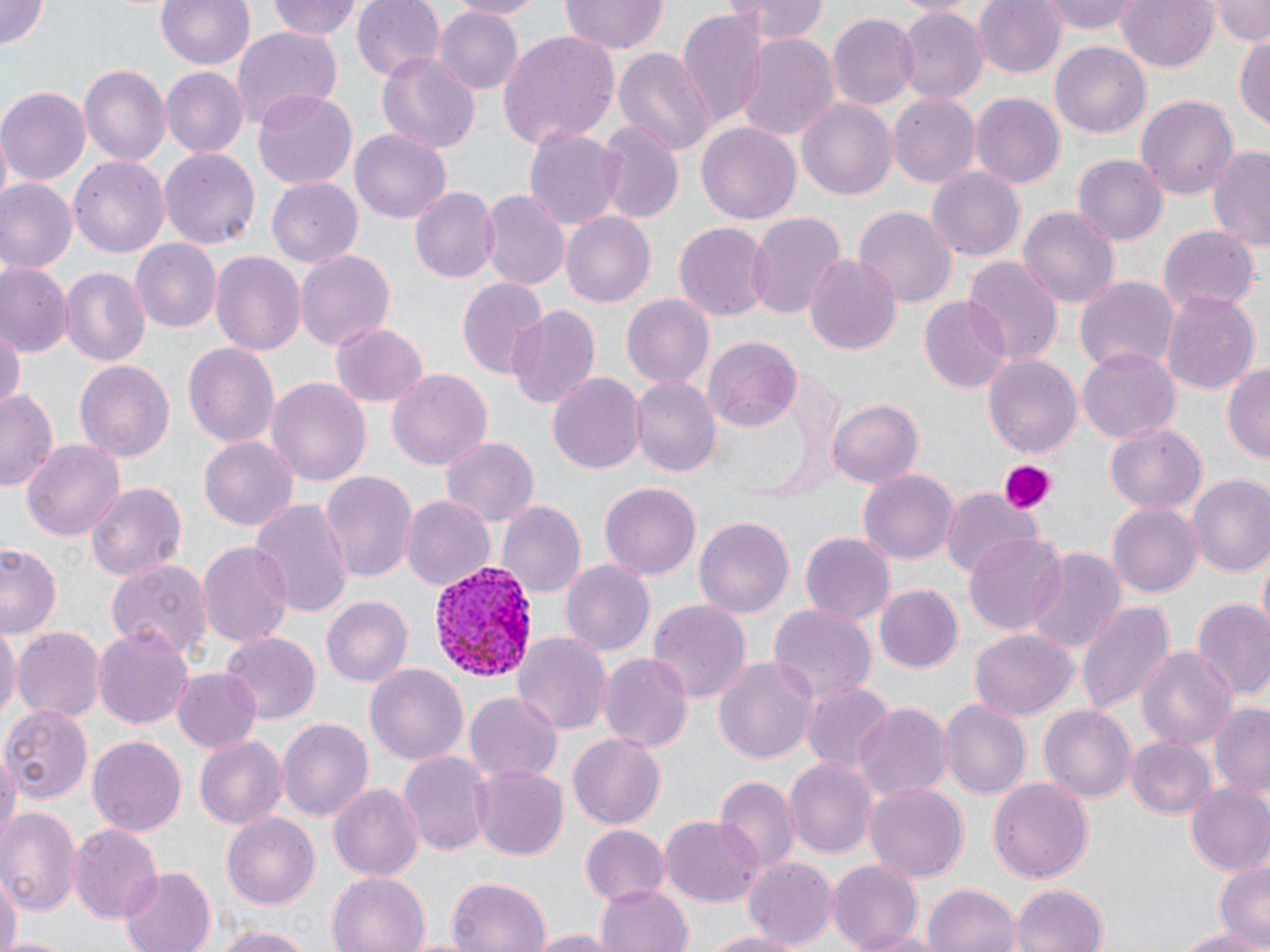
slide-level diagnosis = Plasmodium vivax
uninfected red blood cell locations = approximate bounding boxes as (x1, y1, x2, y2) in pixels: (0, 0, 53, 50), (154, 0, 257, 70), (266, 0, 361, 40), (352, 0, 446, 81), (450, 0, 544, 19), (562, 0, 666, 55), (738, 0, 827, 45), (975, 0, 1067, 79), (1039, 0, 1144, 35), (1116, 0, 1218, 73), (1213, 0, 1270, 44), (675, 5, 768, 125), (896, 5, 988, 104), (436, 7, 523, 94), (827, 13, 918, 112), (231, 25, 343, 128), (1235, 30, 1270, 130), (497, 31, 621, 145), (734, 33, 839, 144), (1051, 41, 1149, 139), (612, 47, 716, 155), (376, 54, 479, 154), (79, 63, 170, 165), (160, 68, 247, 156), (0, 85, 90, 185), (251, 90, 358, 191), (972, 92, 1064, 187), (1136, 94, 1238, 202), (888, 95, 979, 188), (797, 97, 896, 202), (596, 120, 685, 225), (697, 122, 801, 225), (524, 124, 624, 230), (350, 129, 453, 225), (1207, 146, 1270, 252), (160, 147, 259, 250), (70, 154, 168, 254), (1074, 155, 1167, 246), (926, 166, 1025, 262), (266, 177, 363, 270), (1, 180, 76, 273), (410, 187, 499, 283), (481, 189, 569, 289), (854, 206, 957, 308), (1019, 206, 1119, 309), (562, 212, 656, 308), (744, 212, 847, 322), (674, 222, 769, 321), (1157, 224, 1259, 317), (132, 240, 222, 332), (209, 250, 307, 355), (294, 251, 394, 349), (804, 253, 902, 354), (960, 256, 1063, 368), (2, 265, 69, 357), (59, 266, 150, 368), (456, 276, 549, 382), (1075, 276, 1178, 374), (1162, 291, 1259, 395), (623, 295, 713, 389), (920, 296, 1012, 393), (507, 305, 600, 411), (0, 319, 23, 417), (329, 321, 429, 406), (704, 335, 801, 431), (182, 340, 281, 452), (1077, 346, 1181, 443), (982, 351, 1084, 460), (73, 357, 175, 461), (1223, 360, 1270, 463), (387, 369, 492, 474), (548, 371, 645, 478), (630, 375, 719, 477), (266, 377, 372, 488), (0, 389, 59, 493), (829, 398, 923, 487), (1105, 422, 1207, 515), (440, 436, 540, 529), (200, 437, 296, 532), (22, 439, 124, 543), (859, 469, 957, 563), (321, 470, 417, 582), (1187, 475, 1270, 578), (85, 479, 187, 583), (600, 482, 701, 580), (942, 487, 1042, 582), (403, 496, 494, 594), (250, 499, 352, 618), (499, 502, 586, 601), (1107, 502, 1201, 599), (694, 515, 793, 617), (801, 533, 895, 623), (962, 534, 1068, 636), (197, 540, 294, 650), (0, 544, 63, 639), (1020, 546, 1128, 658), (1256, 555, 1269, 628), (105, 556, 213, 660), (561, 558, 655, 655), (873, 585, 961, 673), (322, 596, 412, 688), (1075, 598, 1173, 717), (646, 599, 752, 704), (1193, 600, 1270, 700), (766, 606, 876, 706), (0, 624, 19, 724), (93, 624, 195, 730), (12, 627, 104, 724), (514, 631, 612, 735), (970, 631, 1077, 722), (221, 633, 320, 722), (1138, 645, 1236, 750), (598, 649, 692, 751), (713, 653, 819, 768), (364, 663, 468, 766), (170, 668, 262, 755), (803, 682, 894, 773), (466, 693, 563, 785), (941, 699, 1029, 798), (853, 701, 953, 802), (1039, 703, 1135, 803), (1207, 703, 1270, 801), (1, 704, 92, 803), (278, 716, 374, 825), (568, 733, 666, 829), (194, 734, 288, 829), (88, 736, 185, 838), (1125, 737, 1216, 819), (1, 744, 17, 852), (399, 750, 491, 857), (784, 757, 879, 860), (471, 763, 567, 858), (711, 773, 799, 874), (990, 777, 1093, 882), (329, 782, 425, 882), (864, 783, 969, 882), (1185, 783, 1270, 877), (0, 807, 82, 918), (223, 814, 320, 907), (660, 816, 762, 906), (71, 822, 163, 924), (581, 824, 669, 908), (1215, 855, 1270, 947), (744, 857, 836, 949), (826, 859, 922, 949), (118, 867, 215, 952), (326, 870, 432, 952), (1, 873, 19, 952), (447, 877, 552, 952), (596, 883, 692, 952), (924, 883, 1021, 952), (1008, 885, 1109, 952), (206, 925, 318, 951), (1168, 927, 1270, 950), (856, 928, 945, 952), (527, 929, 613, 951), (701, 930, 809, 952)
Plasmodium vivax-infected red blood cell locations = approximate bounding boxes as (x1, y1, x2, y2) in pixels: (431, 558, 536, 686)
preparation = thin blood film
platelet locations = approximate bounding boxes as (x1, y1, x2, y2) in pixels: (996, 458, 1059, 513)
field of view = single
image size = 1270×952 pixels
magnification = 1000x
modality = light microscopy
stain = May-Grünwald-Giemsa